Comment on the morphology of the red blood cells.
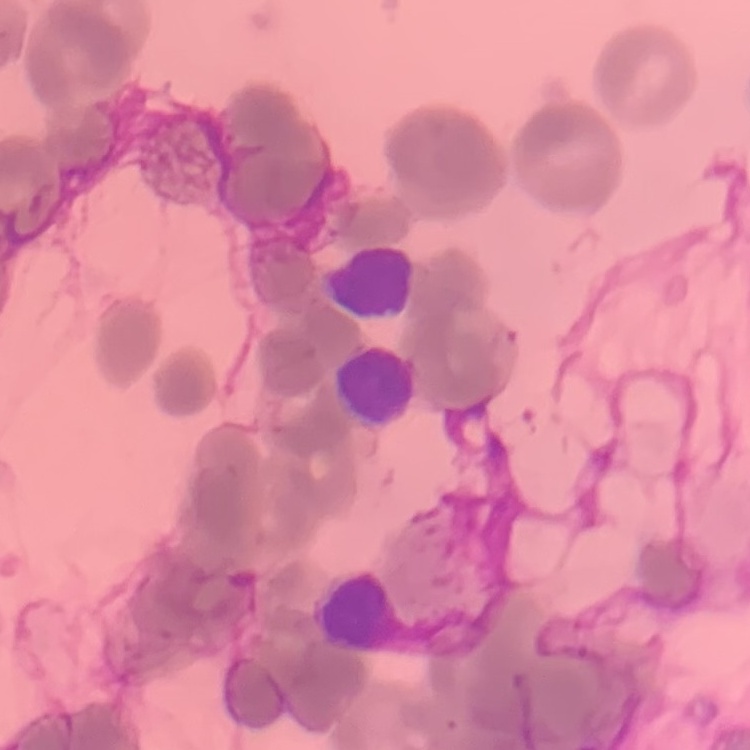
Rouleaux formation.

image type = one tile cut from a larger photomicrograph
stain = Field's or Giemsa
preparation = thin blood film